Assess this cell for malaria.
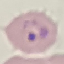
Parasitized.

{
  "preparation": "thin smear",
  "stain": "Giemsa",
  "image_type": "cell patch, automatically extracted from a larger field of view and resized to 64 × 64 pixels",
  "capture": "smartphone through the microscope eyepiece"
}